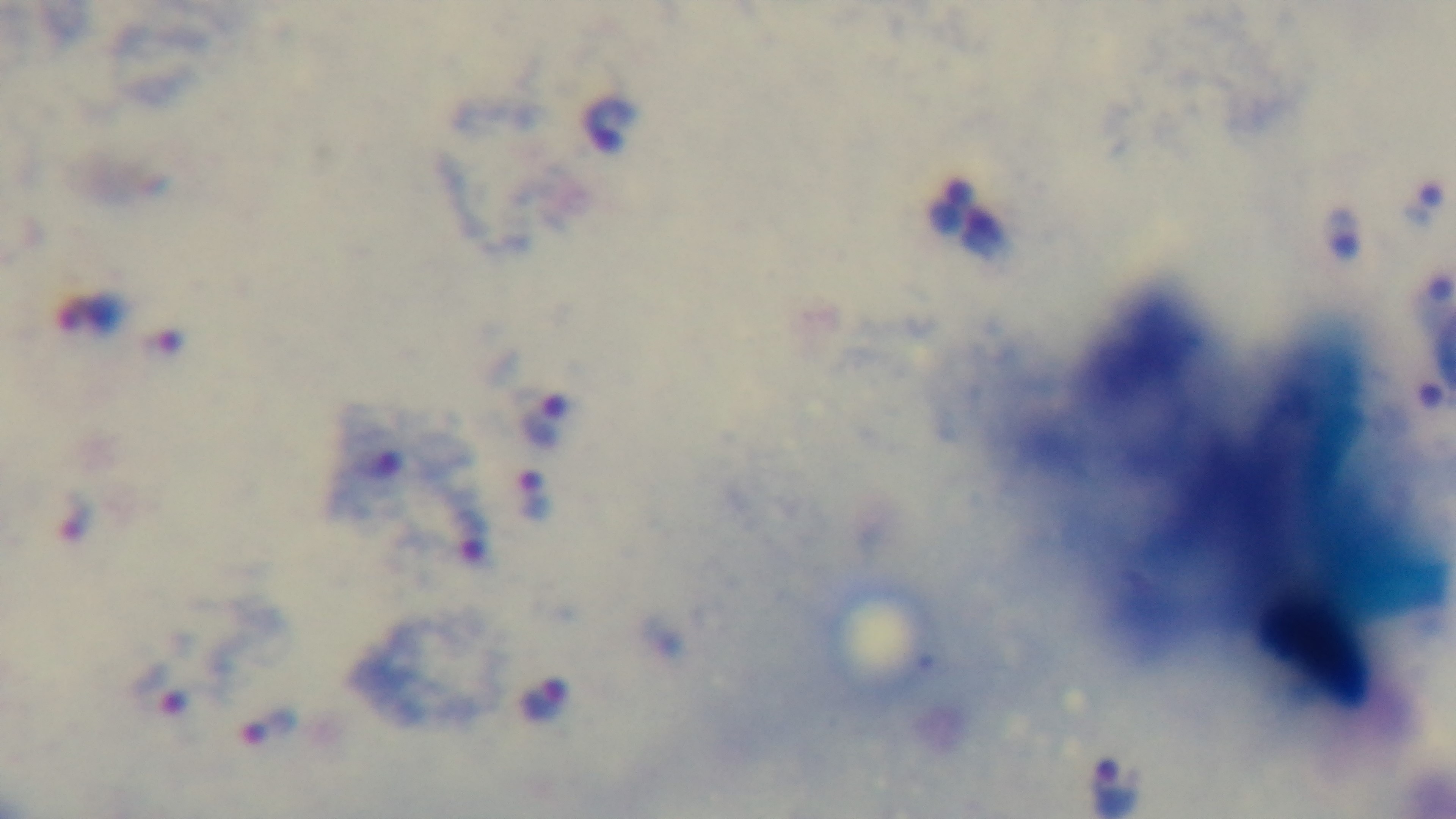 Photomicrograph. Single field of view. Oil-immersion objective, 100x. Preparation: thick. Malaria status: infected. Giemsa stain. Mounted 4K digital camera.